Identify the parasite.
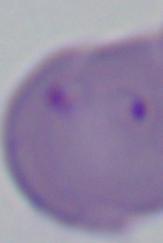
This is Babesia.

Captured at 1000x magnification. Micrograph.